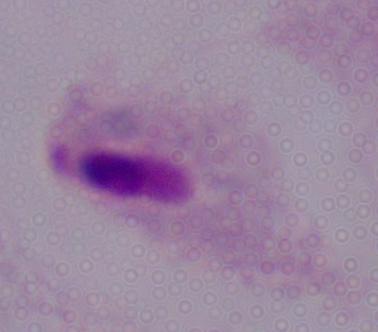 Micrograph. A trichomonad is shown. Captured at 1000x magnification.